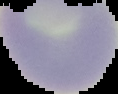
image type = segmented cell region with the area outside set to black
image size = 118×94 pixels
preparation = thin blood film
result = no malaria parasites detected